Identify the blood parasite species.
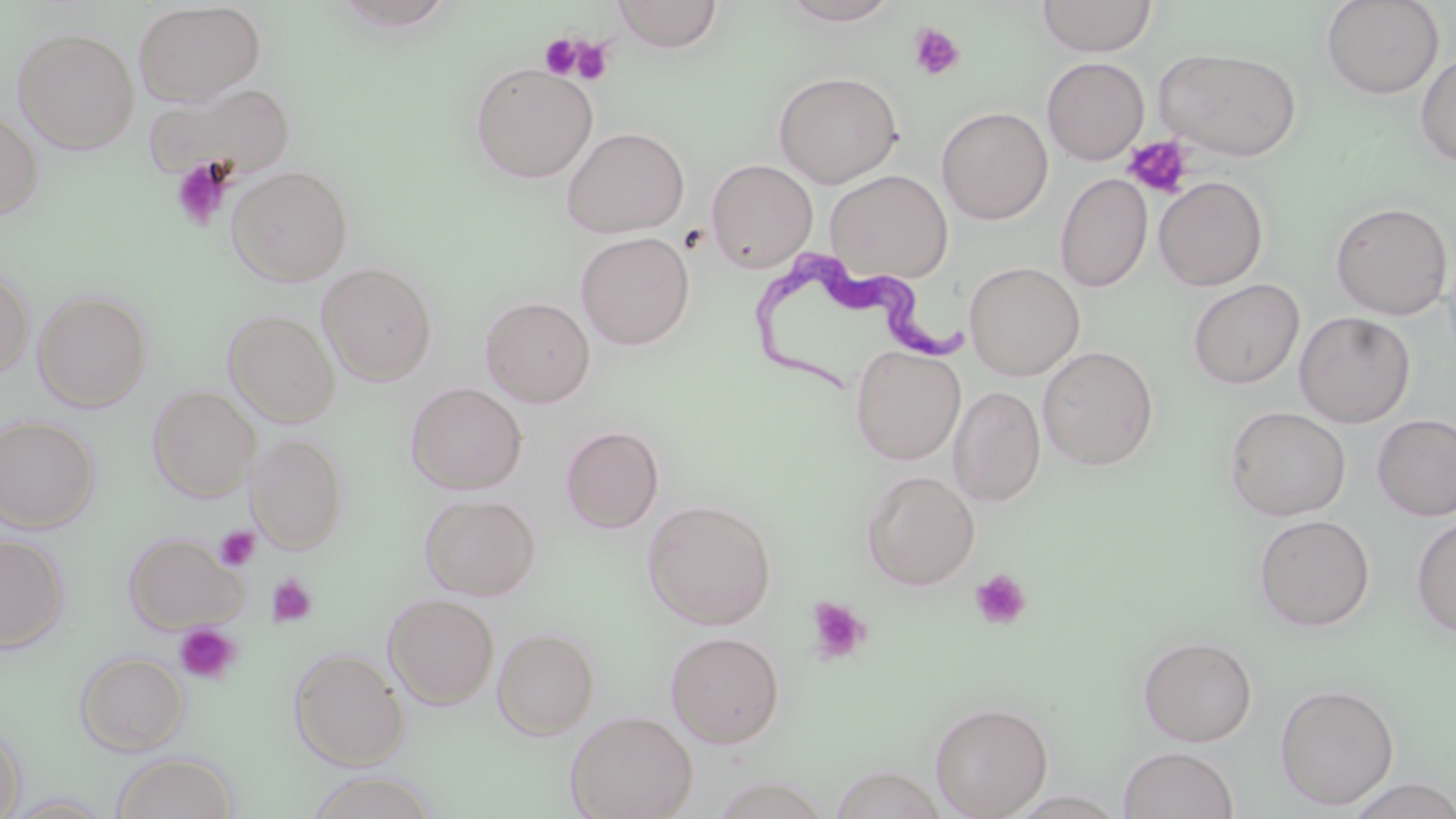
Trypanosoma brucei.

Approximate bounding boxes as (x1, y1, x2, y2) in pixels. Trypanosoma brucei locations: (749, 246, 989, 396). Uninfected red blood cell locations: (612, 0, 724, 52), (778, 0, 902, 26), (1036, 0, 1157, 57), (1321, 0, 1444, 99), (133, 2, 265, 106), (12, 27, 139, 154), (1154, 47, 1303, 161), (1415, 54, 1456, 167), (1042, 57, 1149, 165), (469, 63, 597, 183), (774, 71, 902, 188), (143, 80, 296, 181), (937, 107, 1053, 224), (0, 108, 44, 222), (562, 127, 689, 237), (706, 159, 817, 272), (227, 165, 353, 286), (825, 170, 953, 283), (1055, 173, 1152, 292), (1154, 176, 1268, 291), (1330, 201, 1453, 319), (576, 231, 695, 350), (965, 262, 1085, 381), (317, 263, 437, 385), (0, 266, 34, 380), (1188, 279, 1304, 390), (33, 290, 153, 411), (480, 296, 595, 408), (224, 309, 340, 427), (1295, 311, 1416, 427), (850, 345, 966, 465), (1038, 346, 1158, 470), (406, 382, 527, 494), (148, 385, 260, 501), (948, 386, 1046, 506), (1224, 406, 1350, 521), (1372, 413, 1456, 521), (0, 415, 99, 533), (560, 425, 664, 533), (247, 433, 348, 553), (861, 470, 979, 590), (419, 493, 541, 600), (642, 499, 777, 630), (1253, 514, 1375, 632), (1411, 516, 1456, 637), (123, 532, 245, 633), (0, 533, 69, 653), (384, 593, 499, 709), (493, 628, 599, 739), (666, 631, 784, 747), (1138, 635, 1257, 746), (289, 647, 409, 770), (75, 650, 190, 755), (1275, 683, 1399, 809), (929, 701, 1053, 818), (565, 710, 698, 819), (0, 723, 26, 819), (1118, 746, 1240, 819), (110, 752, 239, 819), (828, 765, 948, 819), (305, 771, 438, 819), (1343, 776, 1456, 819), (3, 793, 117, 817). Platelet locations: (909, 23, 965, 80), (540, 34, 582, 79), (570, 37, 614, 86), (1123, 135, 1193, 198), (171, 158, 233, 231), (214, 525, 260, 571), (970, 569, 1032, 630), (265, 573, 318, 627), (806, 596, 872, 665), (174, 623, 242, 686). Optical microscopy. Single field of view. 1000x magnification. May-Grünwald-Giemsa stain. Thin blood smear. Image is 1456×819 pixels.